Assess this cell for malaria.
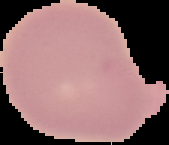

It is uninfected.

Summary:
  - Image type: cell region segmented out of the field of view; surrounding area masked to black
  - Preparation: thin blood film
  - Image size: 169×145 pixels